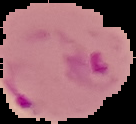
Summary:
  - Image type: segmented cell region on a black background
  - Malaria status: parasitized
  - Image size: 136×124 pixels
  - Preparation: thin blood film